Report the malaria status of this cell.
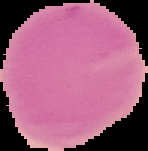

It is uninfected.

Summary:
  - Image type: cell region segmented out of the field of view; surrounding area masked to black
  - Image size: 148×151 pixels
  - Preparation: thin blood smear